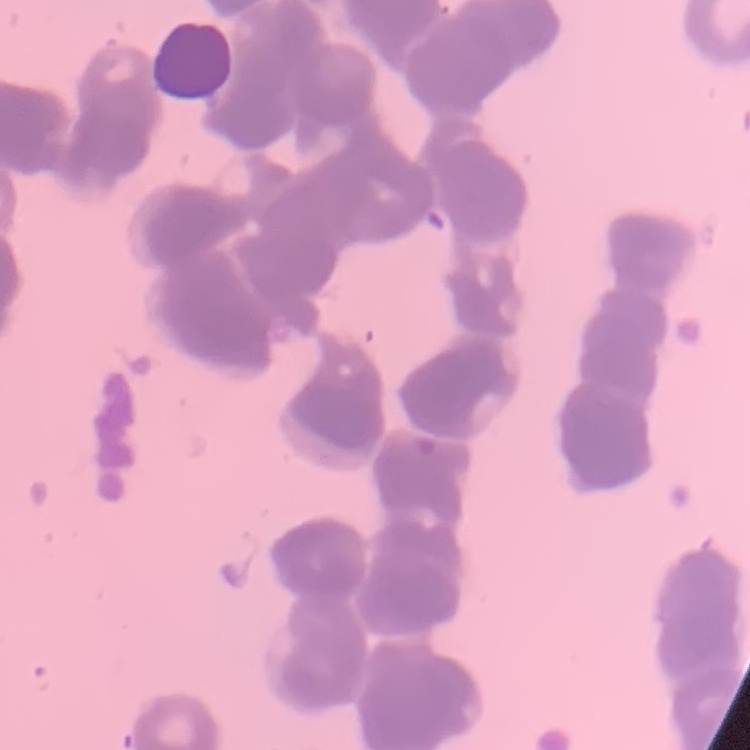 The red blood cells show rouleaux formation. Square crop of a larger photomicrograph. Stained with either Field's or Giemsa. Thin peripheral smear.